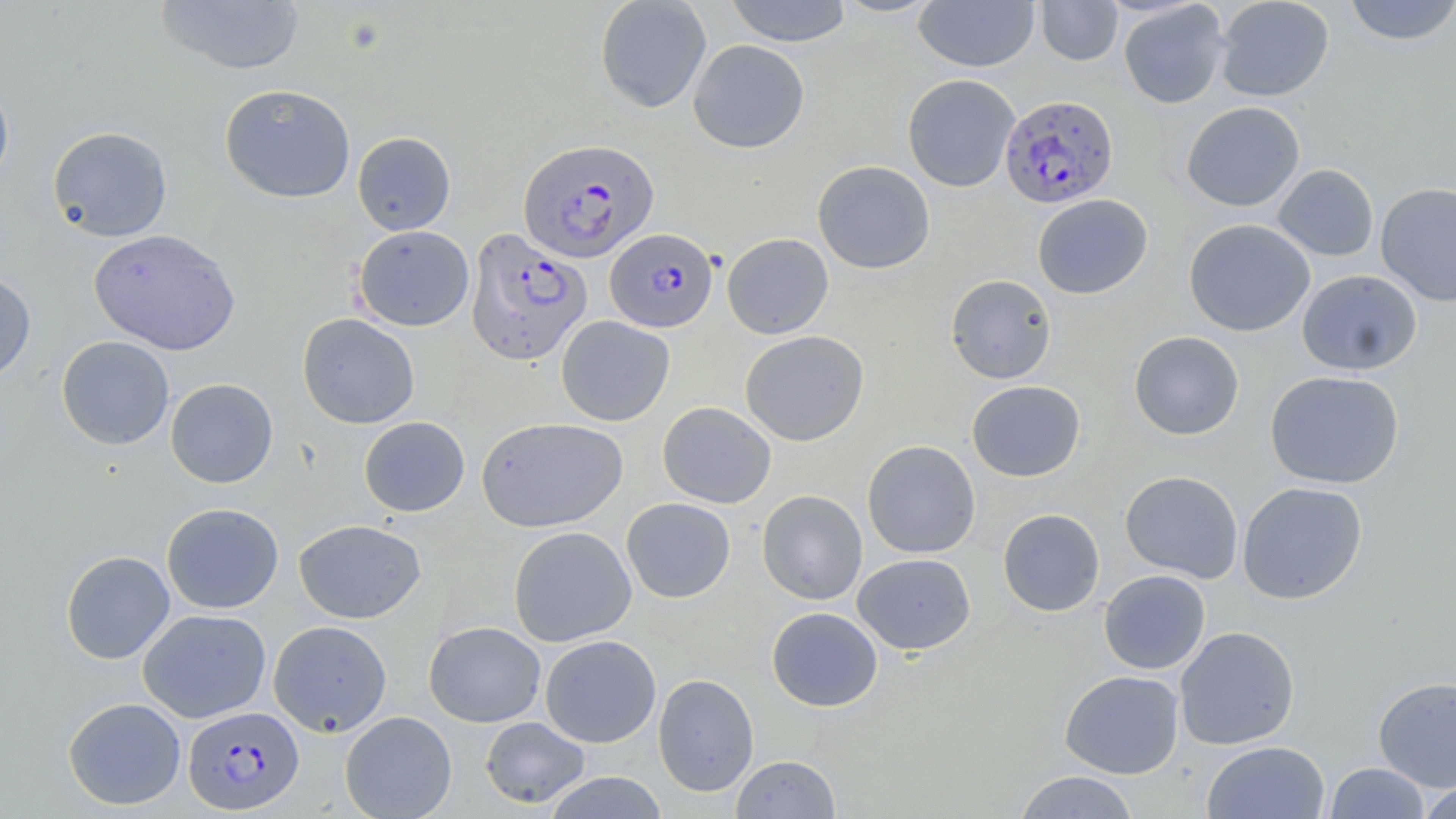

Approximate bounding boxes as (x1,y1)-(x2,y2) corner pairs in pixels. Plasmodium falciparum-infected red blood cell locations: (999,94)-(1119,208), (518,137)-(659,264), (465,228)-(593,366), (605,228)-(718,332), (182,705)-(304,814). Uninfected red blood cell locations: (155,0)-(306,75), (594,0)-(712,113), (724,0)-(853,47), (830,0)-(944,18), (1036,0)-(1123,66), (1215,0)-(1334,102), (1344,0)-(1456,46), (914,1)-(1039,71), (1118,2)-(1231,109), (688,39)-(810,153), (902,74)-(1021,192), (0,77)-(14,192), (219,83)-(356,203), (1181,102)-(1305,212), (47,126)-(173,242), (352,132)-(456,235), (812,160)-(935,274), (1273,163)-(1379,262), (1376,183)-(1456,306), (1032,194)-(1153,298), (1184,219)-(1315,336), (353,225)-(474,331), (89,228)-(241,355), (722,233)-(833,339), (1297,270)-(1422,376), (0,271)-(36,385), (945,274)-(1056,384), (297,313)-(420,429), (556,316)-(674,426), (740,330)-(869,446), (1129,331)-(1244,440), (56,336)-(174,450), (1265,370)-(1404,489), (165,378)-(278,488), (967,380)-(1085,482), (657,401)-(776,508), (358,416)-(470,517), (476,417)-(628,532), (862,441)-(980,558), (1120,470)-(1244,584), (1237,482)-(1368,605), (756,489)-(868,605), (621,497)-(736,603), (161,503)-(284,613), (997,508)-(1105,616), (294,519)-(426,623), (508,526)-(636,647), (60,550)-(175,664), (852,552)-(976,655), (1099,570)-(1211,674), (766,607)-(883,712), (138,608)-(271,723), (268,620)-(392,736), (424,621)-(545,727), (1174,626)-(1300,750), (540,635)-(661,748), (1059,670)-(1185,778), (653,673)-(759,796), (1373,676)-(1456,791), (63,696)-(186,810), (340,711)-(457,819), (480,716)-(590,809), (1202,741)-(1330,819), (731,754)-(841,818), (1324,762)-(1430,818), (1013,770)-(1141,818), (543,771)-(669,819), (1417,780)-(1456,819). Slide-level diagnosis: Plasmodium falciparum. Image is 1456×819 pixels. One field of a larger specimen. Light microscopy. Captured at 1000x magnification. May-Grünwald-Giemsa stain. Thin blood smear.